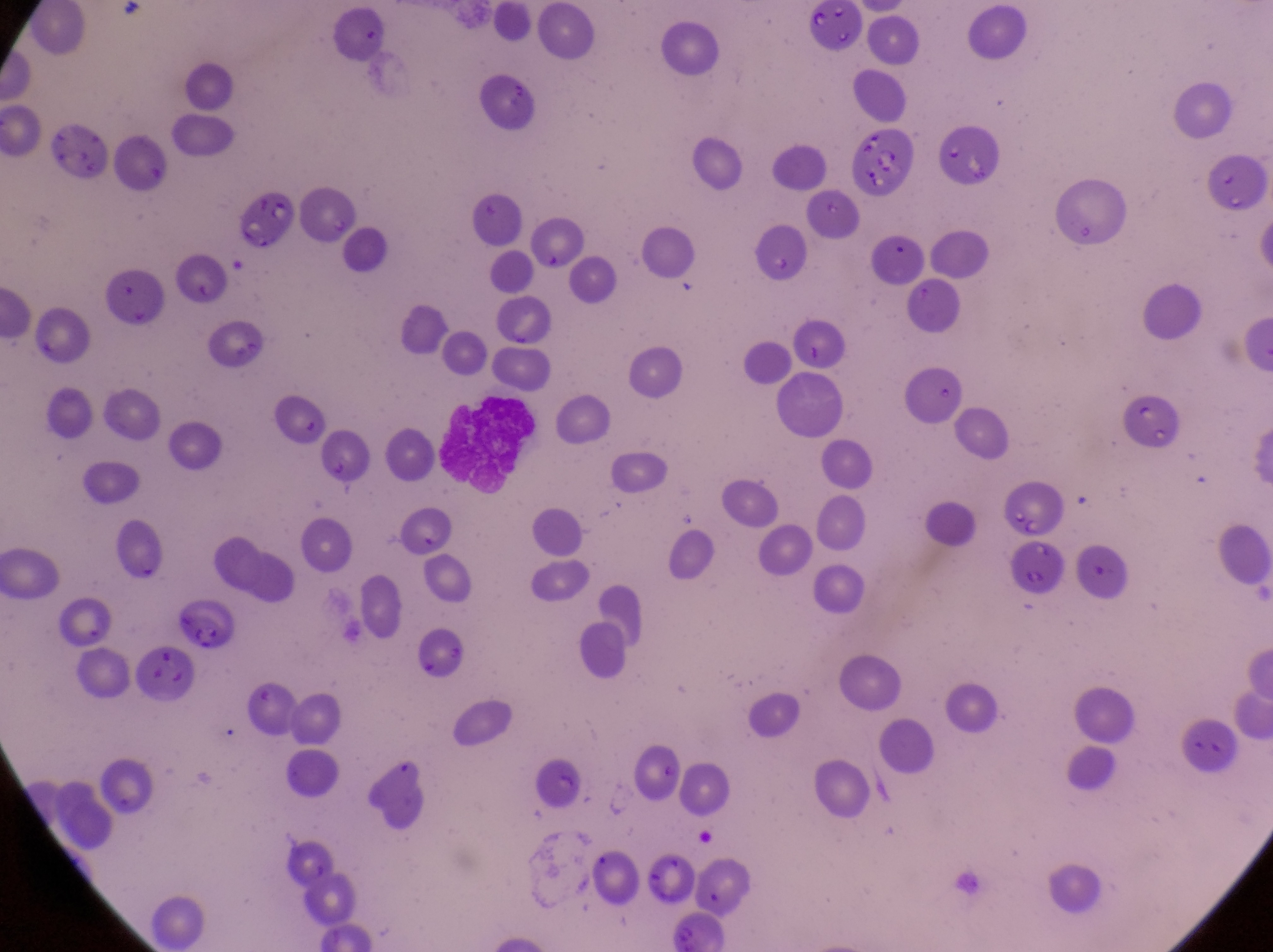

Approximate bounding boxes as [left, top, right, bottom] in pixels.
Summary:
  - Parasitised red blood cell locations: [998, 491, 1065, 538]
  - Artifact (platelet-like body, stain precipitate, or debris) locations: [45, 115, 112, 185], [849, 123, 919, 200], [234, 188, 297, 253], [756, 225, 809, 280], [439, 397, 539, 490], [130, 651, 197, 699]
  - Image size: 1273×952 pixels
  - Preparation: thin blood smear
  - Capture: smartphone photograph through the eyepiece of an Olympus CX-23 microscope
  - Magnification: 1000x
  - Field of view: single
  - Country: Uganda